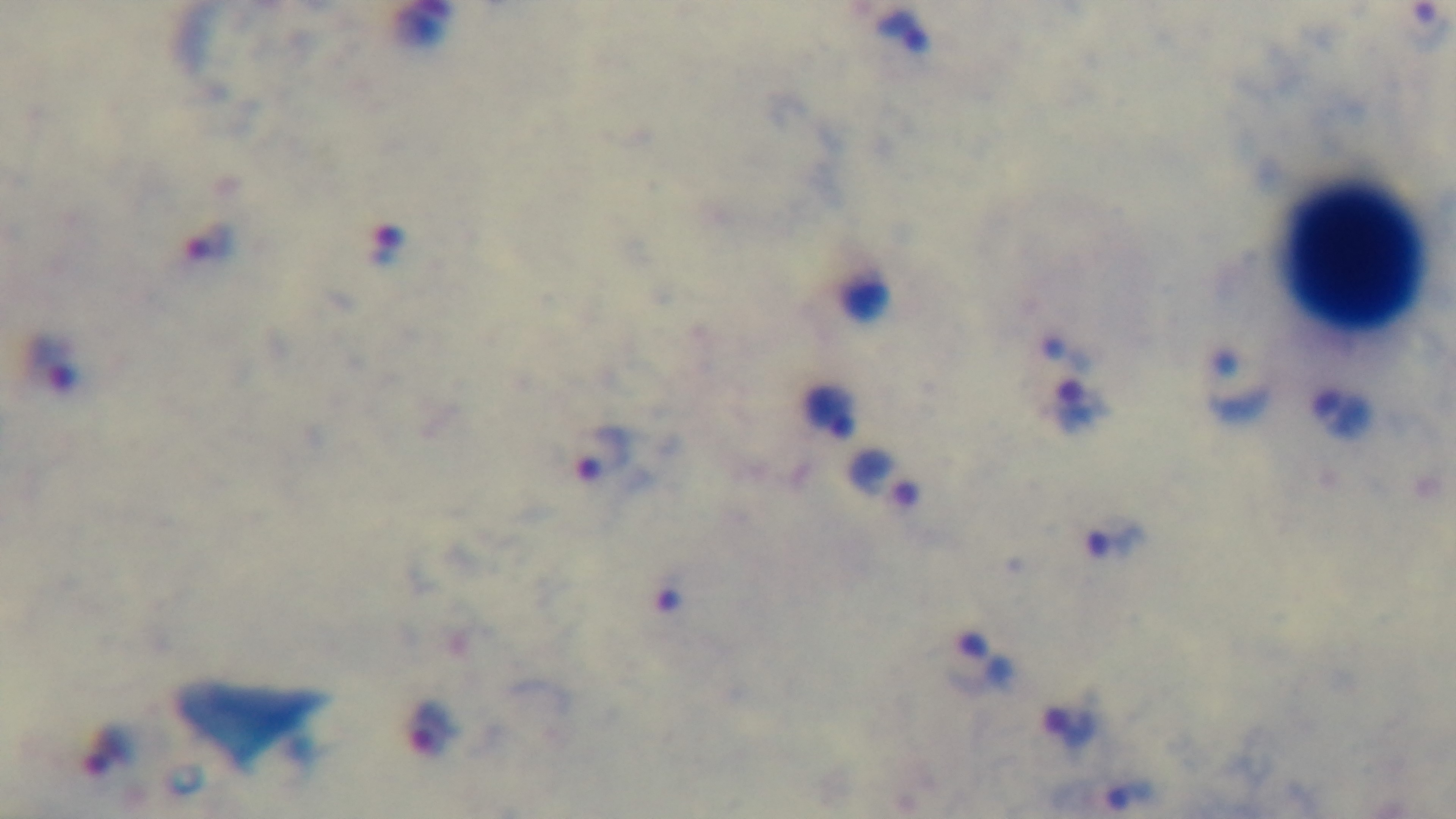

Mounted 4K digital camera. Preparation: thick blood film. Malaria status: infected. Photomicrograph. Oil-immersion objective, 100x. One field from the slide. Giemsa-stained.